Report the malaria status of this cell.
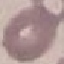
It is uninfected.

image type = cell patch, automatically extracted from a larger field of view and resized to 64 × 64 pixels
capture = smartphone camera at the microscope eyepiece
stain = Giemsa
preparation = thin blood film